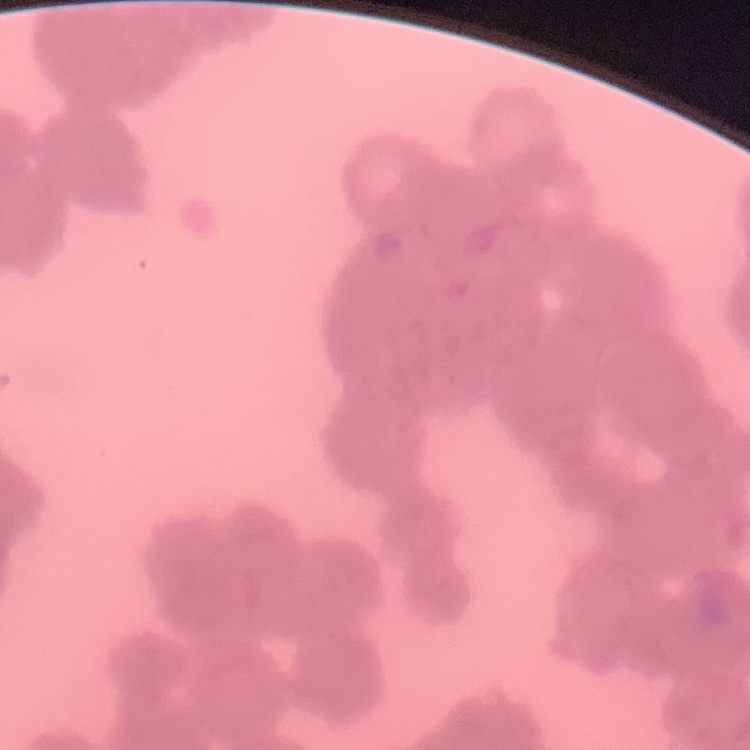
Summary:
  - Red blood cell morphology: rouleaux formation
  - Image type: one tile cut from a larger photomicrograph
  - Stain: Field's or Giemsa
  - Preparation: thin blood smear